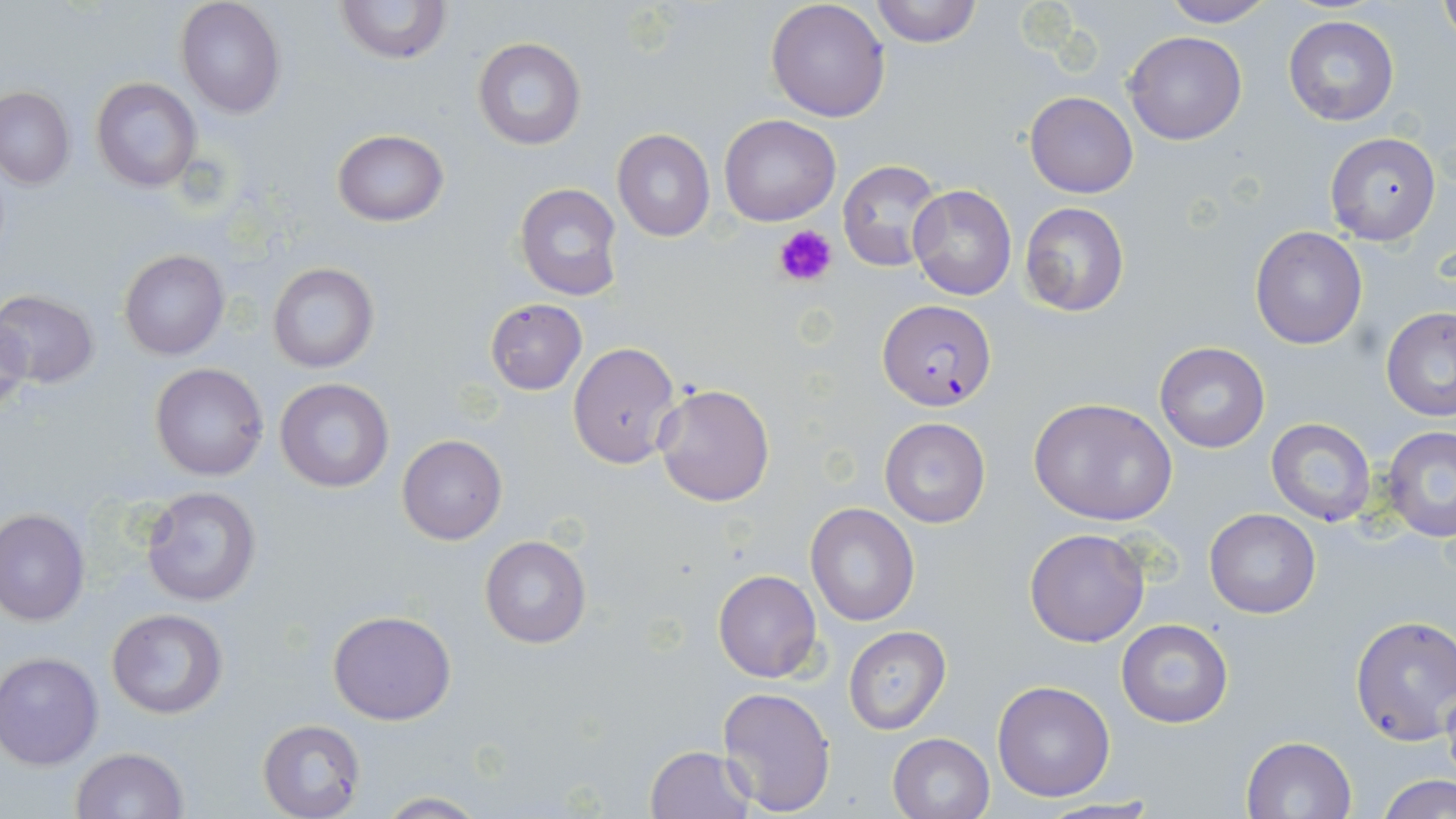
Summary:
  - Coordinate format: approximate bounding boxes as named x1/y1/x2/y2 corners in pixels
  - Uninfected red blood cell locations: (x1=337, y1=0, x2=451, y2=67), (x1=766, y1=0, x2=890, y2=121), (x1=868, y1=0, x2=982, y2=46), (x1=1155, y1=0, x2=1277, y2=27), (x1=1438, y1=0, x2=1456, y2=50), (x1=175, y1=1, x2=284, y2=117), (x1=1283, y1=15, x2=1399, y2=127), (x1=1124, y1=30, x2=1246, y2=145), (x1=472, y1=37, x2=587, y2=152), (x1=90, y1=77, x2=201, y2=191), (x1=0, y1=87, x2=74, y2=188), (x1=1024, y1=90, x2=1138, y2=198), (x1=718, y1=113, x2=840, y2=226), (x1=331, y1=129, x2=449, y2=227), (x1=612, y1=129, x2=715, y2=241), (x1=1324, y1=132, x2=1443, y2=246), (x1=838, y1=159, x2=946, y2=274), (x1=513, y1=181, x2=623, y2=302), (x1=907, y1=183, x2=1017, y2=300), (x1=1019, y1=201, x2=1130, y2=315), (x1=1249, y1=225, x2=1367, y2=349), (x1=120, y1=249, x2=230, y2=361), (x1=266, y1=261, x2=379, y2=375), (x1=1, y1=290, x2=100, y2=388), (x1=484, y1=299, x2=587, y2=394), (x1=0, y1=307, x2=30, y2=423), (x1=1381, y1=307, x2=1456, y2=421), (x1=1153, y1=341, x2=1270, y2=453), (x1=567, y1=342, x2=682, y2=468), (x1=151, y1=362, x2=269, y2=482), (x1=274, y1=378, x2=394, y2=492), (x1=653, y1=383, x2=775, y2=507), (x1=1028, y1=397, x2=1177, y2=525), (x1=878, y1=417, x2=990, y2=529), (x1=1266, y1=417, x2=1378, y2=526), (x1=1380, y1=426, x2=1456, y2=542), (x1=397, y1=434, x2=506, y2=544), (x1=140, y1=485, x2=264, y2=608), (x1=805, y1=503, x2=920, y2=626), (x1=0, y1=508, x2=89, y2=627), (x1=1204, y1=508, x2=1320, y2=619), (x1=1023, y1=528, x2=1150, y2=647), (x1=480, y1=535, x2=592, y2=650), (x1=712, y1=569, x2=822, y2=683), (x1=106, y1=608, x2=229, y2=718), (x1=328, y1=610, x2=457, y2=725), (x1=1349, y1=615, x2=1455, y2=745), (x1=1115, y1=617, x2=1233, y2=729), (x1=843, y1=626, x2=950, y2=734), (x1=1, y1=652, x2=103, y2=769), (x1=992, y1=679, x2=1116, y2=802), (x1=1441, y1=684, x2=1456, y2=789), (x1=716, y1=685, x2=837, y2=814), (x1=258, y1=719, x2=366, y2=819), (x1=888, y1=732, x2=995, y2=819), (x1=1241, y1=735, x2=1356, y2=818), (x1=644, y1=745, x2=758, y2=819), (x1=70, y1=747, x2=188, y2=819), (x1=1378, y1=773, x2=1455, y2=819), (x1=372, y1=793, x2=491, y2=817)
  - Plasmodium falciparum-infected red blood cell locations: (x1=879, y1=300, x2=998, y2=410)
  - Platelet locations: (x1=773, y1=224, x2=836, y2=289)
  - Slide-level diagnosis: Plasmodium falciparum
  - Stain: May-Grünwald-Giemsa
  - Modality: light microscopy
  - Image size: 1456×819 pixels
  - Preparation: thin blood film
  - Magnification: 1000x
  - Field of view: one of a larger specimen